Locate every blood parasite and identify its species.
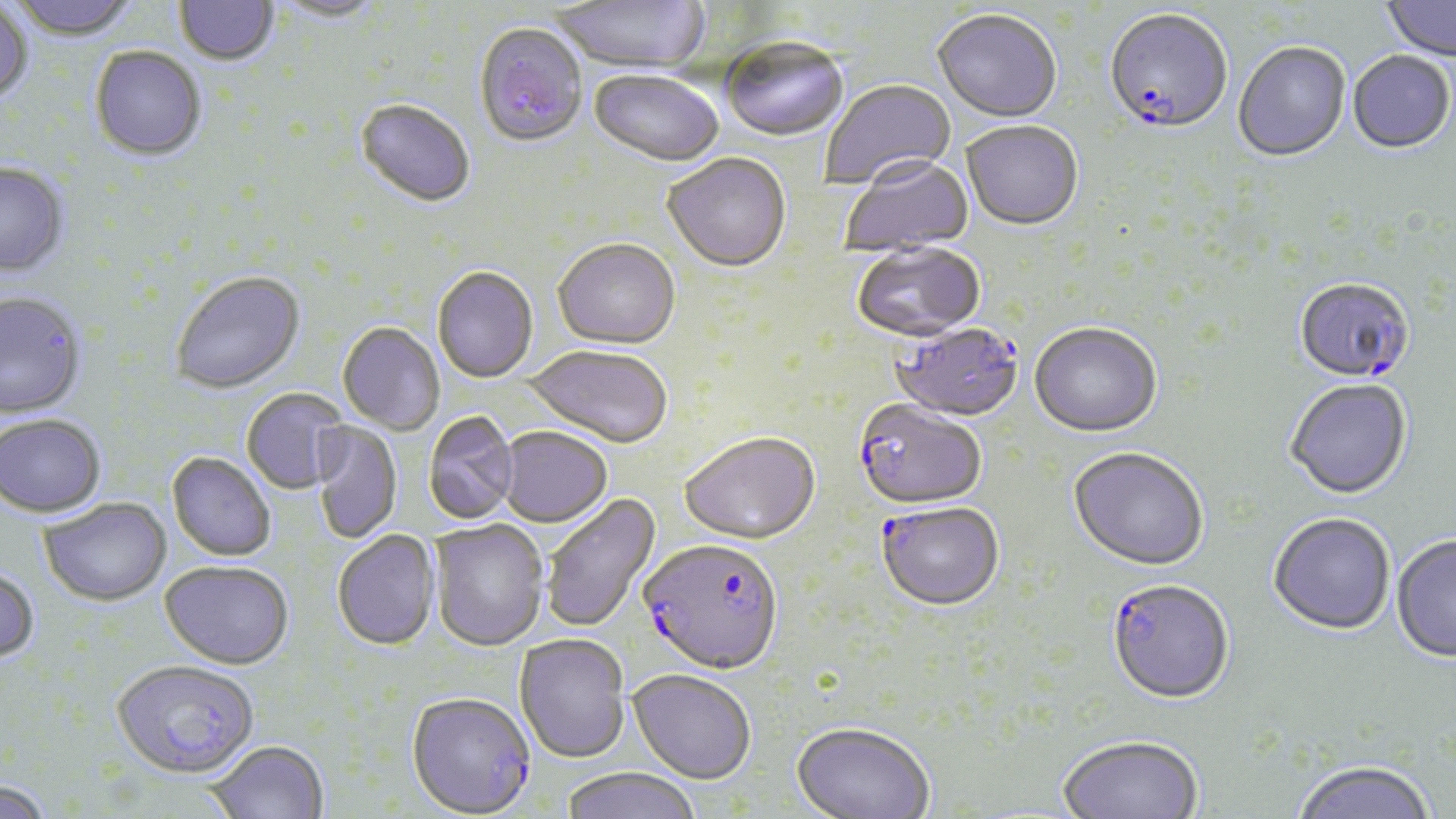
Approximate bounding boxes as (x1, y1, x2, y2) in pixels.
Plasmodium falciparum-infected red blood cells: (1104, 12, 1232, 137), (1293, 279, 1415, 387), (881, 325, 1023, 424), (852, 400, 986, 511), (876, 502, 1004, 612), (639, 538, 785, 675), (1106, 581, 1235, 707), (112, 659, 260, 777), (406, 691, 535, 817).
No Plasmodium ovale, Plasmodium malariae, Plasmodium vivax, Babesia divergens, or Trypanosoma brucei observed.

Uninfected red blood cell locations: (6, 0, 141, 43), (551, 0, 710, 75), (175, 1, 279, 68), (269, 1, 388, 25), (1382, 1, 1455, 63), (0, 3, 33, 107), (932, 11, 1062, 125), (475, 25, 588, 150), (721, 39, 848, 144), (1233, 45, 1350, 164), (89, 48, 207, 163), (1347, 53, 1455, 156), (589, 71, 724, 170), (820, 79, 957, 192), (355, 101, 475, 209), (961, 123, 1083, 233), (662, 155, 791, 274), (840, 158, 974, 258), (0, 164, 69, 278), (552, 240, 680, 351), (851, 244, 985, 344), (432, 267, 538, 383), (170, 273, 306, 395), (0, 292, 87, 420), (337, 323, 445, 435), (1029, 325, 1162, 440), (522, 344, 672, 447), (1284, 380, 1413, 502), (241, 388, 350, 494), (423, 411, 520, 525), (0, 415, 106, 518), (311, 422, 402, 543), (498, 426, 612, 527), (679, 433, 821, 546), (1068, 449, 1208, 573), (167, 452, 276, 561), (540, 492, 661, 634), (39, 498, 171, 606), (1268, 515, 1395, 637), (429, 520, 550, 651), (332, 530, 441, 651), (1391, 536, 1456, 665), (160, 560, 294, 669), (0, 564, 40, 663), (514, 634, 630, 762), (628, 669, 756, 784), (791, 721, 935, 819), (1058, 737, 1203, 819), (206, 740, 329, 819), (1291, 762, 1437, 819), (560, 767, 702, 819), (1, 776, 55, 819). Slide-level diagnosis: Plasmodium falciparum. Optical microscopy. May-Grünwald-Giemsa-stained preparation. Thin blood film. Single field of view. 1000x magnification. Image is 1456×819 pixels.